Assess this cell for malaria.
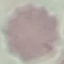
Uninfected.

{
  "preparation": "thin smear",
  "image_type": "cell patch, automatically extracted from a larger field of view and resized to 64 × 64 pixels",
  "stain": "Giemsa",
  "capture": "smartphone camera at the microscope eyepiece"
}